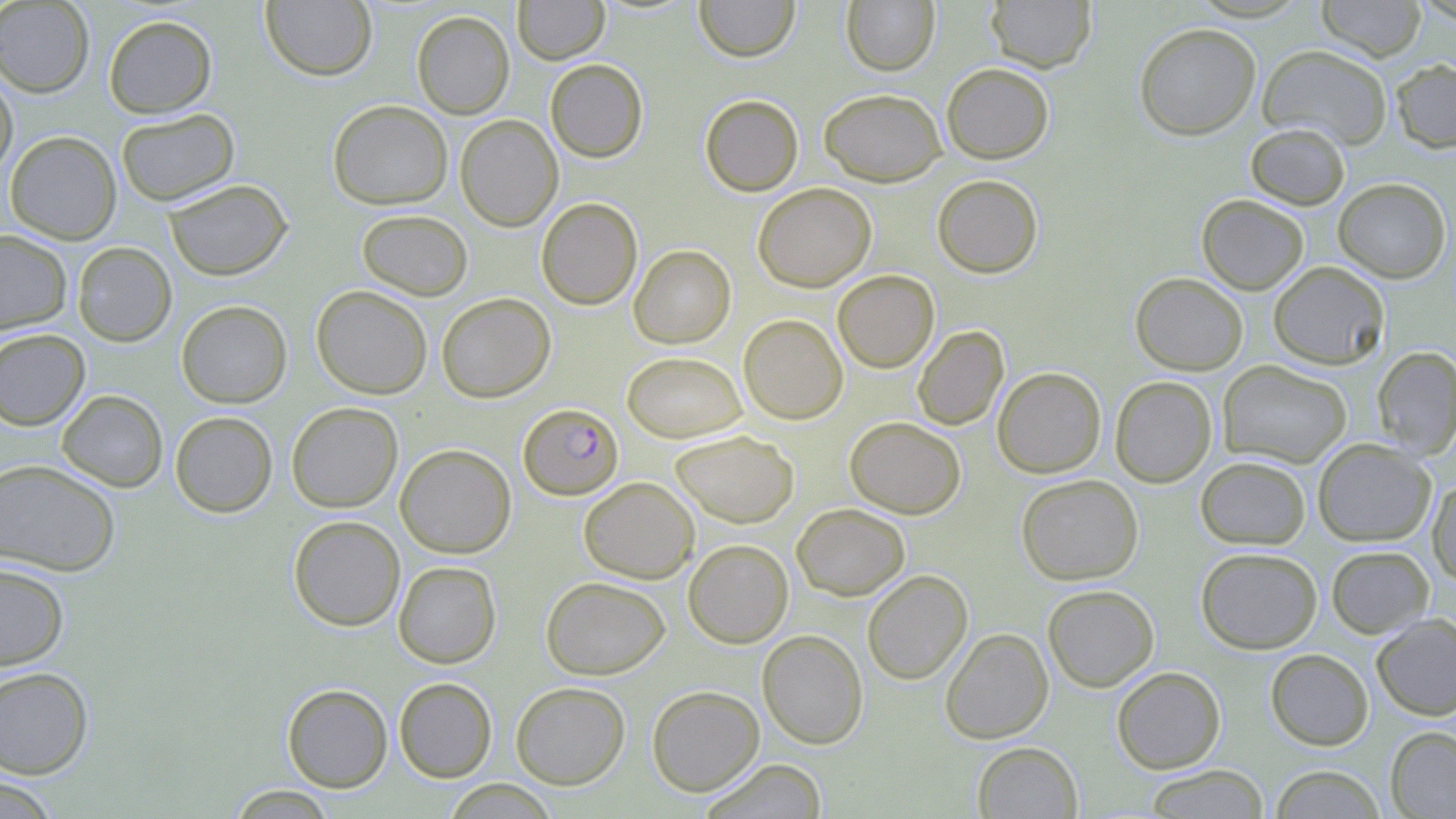

Summary:
  - Coordinate format: approximate bounding boxes as (x1,y1)-(x2,y2) corner pairs in pixels
  - Uninfected red blood cell locations: (260,0)-(377,81), (513,0)-(609,64), (694,0)-(799,62), (1315,0)-(1427,61), (0,1)-(94,97), (841,1)-(940,75), (985,1)-(1096,72), (411,11)-(514,119), (103,14)-(217,118), (1134,22)-(1261,140), (1257,44)-(1393,150), (1390,58)-(1456,153), (545,59)-(648,162), (941,62)-(1054,164), (0,73)-(17,179), (818,87)-(946,186), (700,94)-(803,196), (328,100)-(453,209), (116,109)-(240,206), (455,115)-(563,231), (1245,123)-(1350,209), (5,131)-(121,245), (932,174)-(1043,278), (163,178)-(292,280), (1333,178)-(1451,283), (753,183)-(876,292), (1197,194)-(1309,294), (536,197)-(643,310), (356,209)-(473,301), (0,230)-(72,334), (72,242)-(177,347), (629,245)-(735,348), (1268,261)-(1389,369), (832,270)-(939,373), (1130,272)-(1248,375), (311,285)-(432,399), (436,292)-(555,402), (176,300)-(292,408), (738,314)-(848,425), (912,325)-(1009,431), (0,328)-(90,430), (1372,346)-(1456,458), (622,351)-(748,443), (1218,360)-(1353,468), (992,366)-(1106,478), (1110,376)-(1217,487), (57,390)-(168,492), (286,402)-(403,512), (169,411)-(278,517), (845,416)-(966,519), (670,429)-(799,528), (1313,439)-(1436,546), (395,444)-(516,558), (1195,455)-(1311,549), (0,458)-(121,576), (1016,474)-(1143,585), (1427,475)-(1456,587), (579,477)-(699,583), (791,503)-(910,600), (288,515)-(405,631), (683,539)-(793,648), (1326,545)-(1434,638), (1195,547)-(1322,654), (393,560)-(502,668), (0,562)-(69,670), (862,569)-(973,685), (541,576)-(670,679), (1043,584)-(1159,692), (1371,614)-(1456,720), (940,628)-(1053,743), (757,629)-(868,749), (1265,649)-(1373,750), (0,666)-(94,779), (1111,666)-(1225,774), (394,677)-(497,782), (511,682)-(630,789), (281,683)-(393,792), (646,685)-(764,796), (1386,726)-(1456,819), (972,741)-(1083,818), (700,759)-(828,818), (1144,765)-(1270,818), (1270,765)-(1385,818), (0,776)-(61,819), (438,779)-(560,817), (223,786)-(340,818)
  - Plasmodium falciparum-infected red blood cell locations: (518,403)-(623,500)
  - Slide-level diagnosis: Plasmodium falciparum
  - Image size: 1456×819 pixels
  - Field of view: single
  - Magnification: 1000x
  - Preparation: thin blood film
  - Stain: May-Grünwald-Giemsa
  - Modality: optical microscopy